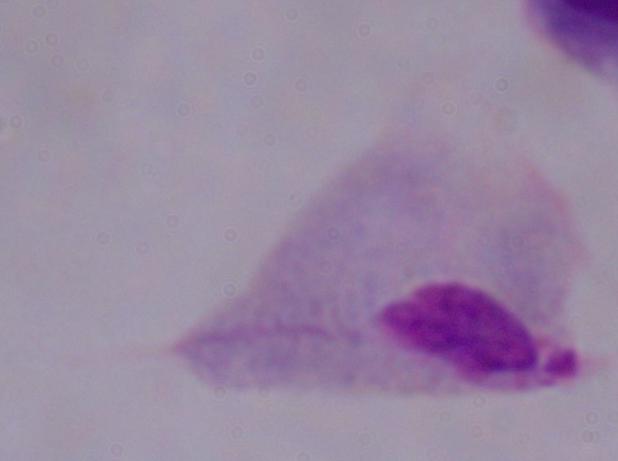 A trichomonad is seen. 1000x magnification. Micrograph.